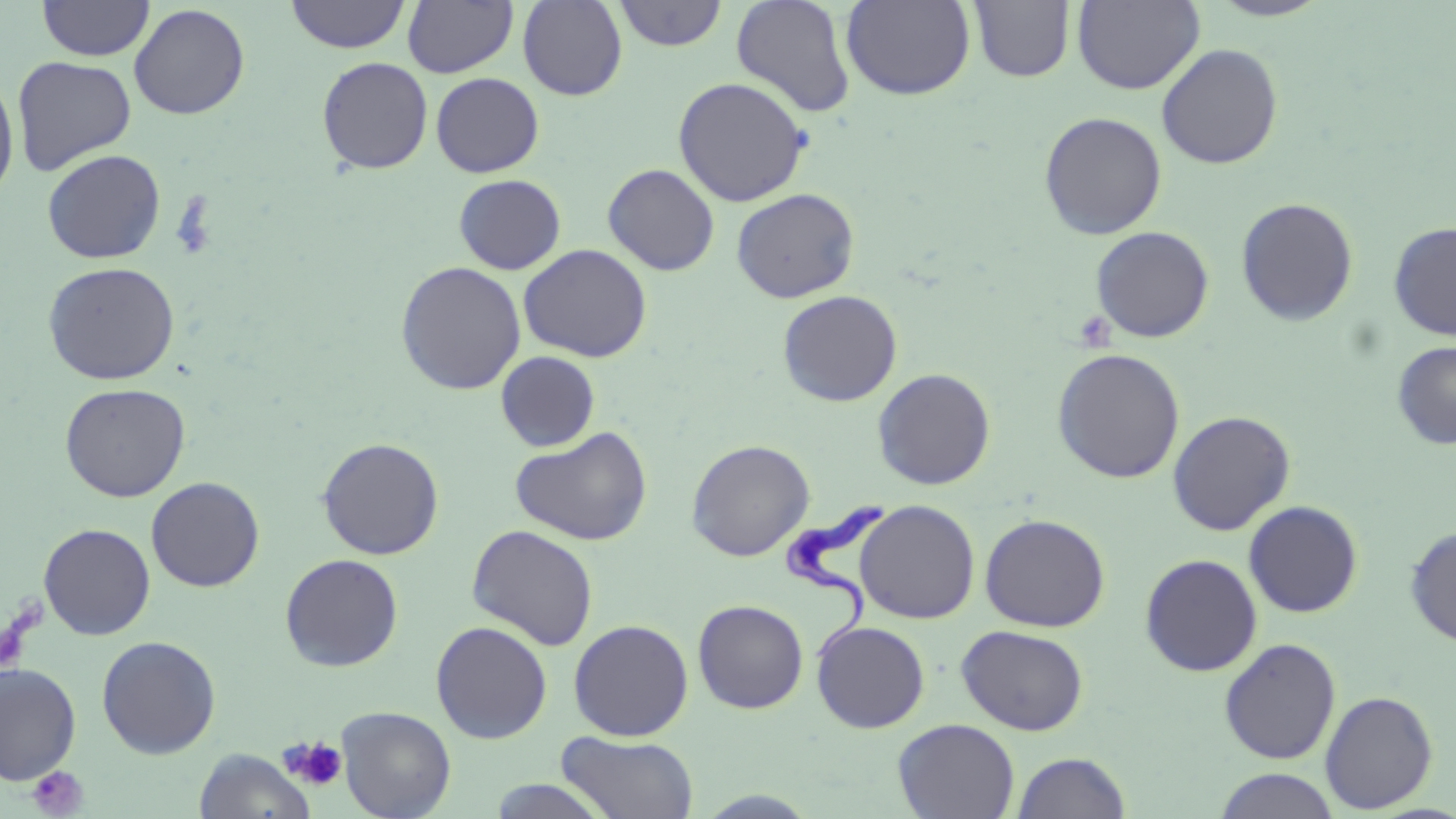
Summary:
  - Coordinate format: approximate bounding boxes as (x1, y1, x2, y2) in pixels
  - Trypanosoma brucei locations: (784, 490, 888, 668)
  - Platelet locations: (279, 736, 348, 793), (28, 765, 87, 817)
  - Uninfected red blood cell locations: (285, 0, 410, 53), (518, 0, 627, 101), (613, 0, 728, 51), (731, 0, 857, 118), (1072, 0, 1204, 94), (1206, 0, 1335, 21), (37, 1, 154, 61), (402, 1, 518, 77), (840, 1, 976, 100), (968, 1, 1075, 83), (129, 4, 250, 120), (1156, 43, 1283, 169), (12, 55, 136, 176), (316, 56, 433, 175), (0, 72, 19, 202), (431, 72, 544, 177), (673, 76, 811, 207), (1039, 111, 1167, 240), (41, 149, 166, 264), (602, 164, 720, 276), (453, 174, 567, 275), (731, 188, 860, 303), (1236, 197, 1358, 326), (1388, 221, 1456, 340), (1090, 226, 1214, 343), (517, 244, 653, 362), (42, 261, 180, 385), (395, 261, 526, 395), (777, 289, 903, 407), (1392, 341, 1456, 450), (1051, 348, 1186, 484), (496, 351, 600, 452), (872, 368, 996, 490), (58, 382, 191, 502), (1167, 410, 1296, 536), (510, 426, 653, 546), (317, 437, 445, 560), (686, 439, 814, 561), (146, 477, 264, 592), (855, 500, 981, 624), (1243, 500, 1363, 618), (980, 514, 1110, 632), (38, 522, 156, 640), (467, 524, 599, 651), (1405, 524, 1456, 648), (1139, 553, 1262, 677), (280, 554, 404, 672), (692, 599, 809, 714), (568, 619, 694, 741), (811, 620, 930, 733), (430, 621, 552, 744), (956, 624, 1089, 736), (96, 635, 221, 759), (1219, 637, 1341, 764), (0, 663, 82, 786), (1320, 690, 1438, 813), (337, 705, 456, 819), (893, 718, 1020, 819), (557, 731, 700, 818), (193, 748, 316, 819), (1010, 751, 1131, 819), (1213, 768, 1342, 819), (487, 779, 615, 818), (689, 788, 824, 817)
  - Slide-level diagnosis: Trypanosoma brucei
  - Image size: 1456×819 pixels
  - Field of view: one of a larger specimen
  - Modality: light microscopy
  - Stain: May-Grünwald-Giemsa
  - Magnification: 1000x
  - Preparation: thin blood film